Locate and identify every blood parasite.
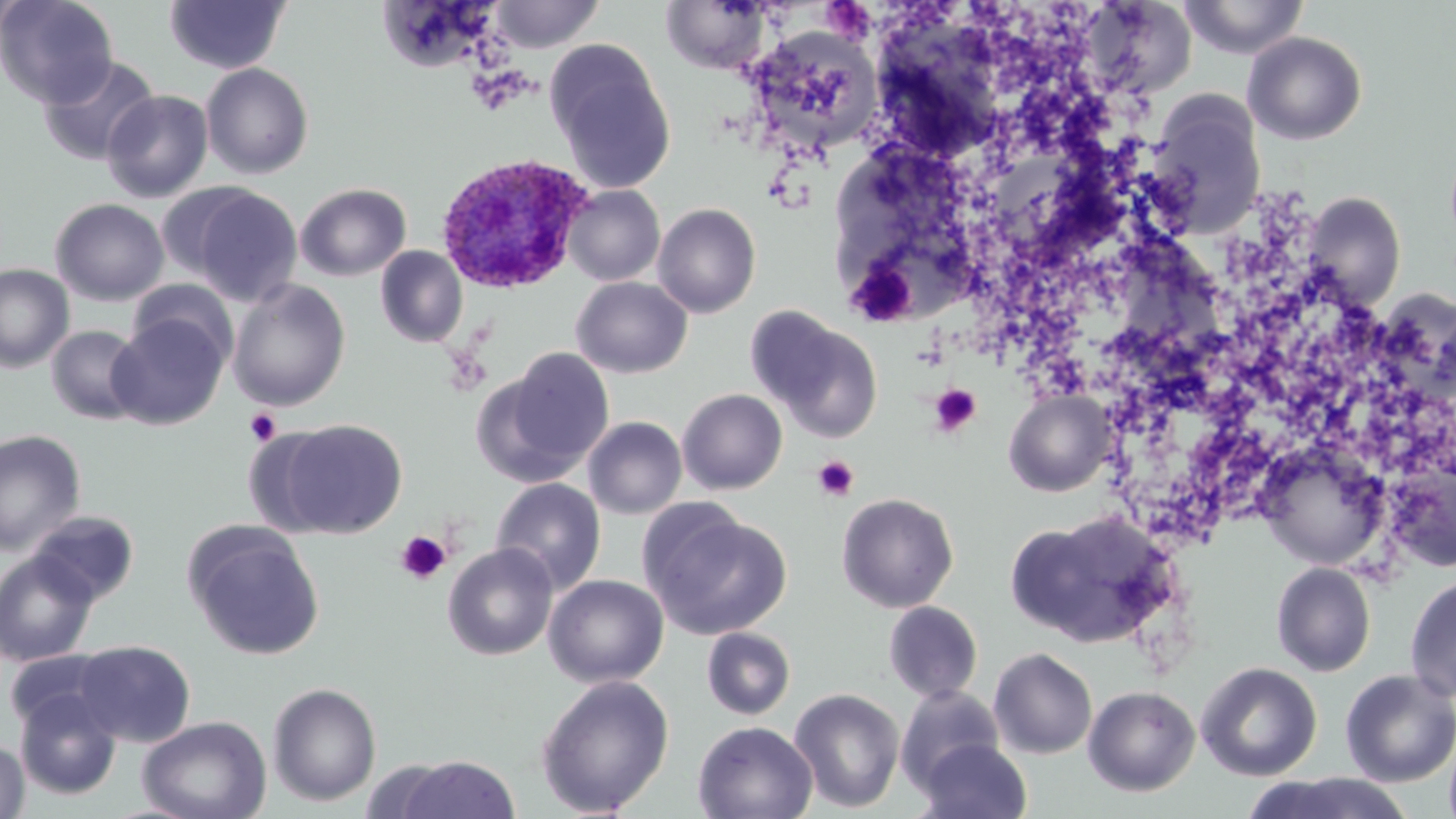
Approximate bounding boxes as (x1, y1, x2, y2) in pixels.
Plasmodium ovale-infected red blood cells: (434, 152, 593, 295).
No Plasmodium falciparum, Plasmodium malariae, Plasmodium vivax, Babesia divergens, or Trypanosoma brucei observed.

slide-level diagnosis = Plasmodium ovale
uninfected red blood cell locations = approximate bounding boxes as (x1, y1, x2, y2) in pixels: (1, 0, 117, 107), (163, 0, 290, 75), (1178, 0, 1310, 60), (489, 1, 604, 52), (660, 1, 769, 74), (744, 25, 883, 154), (1242, 31, 1368, 145), (546, 42, 677, 195), (37, 55, 160, 166), (201, 63, 314, 179), (101, 89, 213, 202), (1148, 98, 1265, 234), (296, 183, 411, 281), (181, 184, 303, 307), (562, 185, 664, 286), (1301, 191, 1406, 311), (50, 198, 169, 306), (653, 203, 761, 318), (375, 245, 468, 347), (0, 263, 74, 373), (571, 277, 692, 378), (128, 280, 239, 371), (227, 280, 351, 411), (751, 309, 884, 441), (107, 312, 229, 430), (45, 324, 146, 425), (489, 348, 615, 481), (678, 389, 787, 494), (583, 417, 687, 519), (272, 418, 408, 538), (0, 429, 86, 555), (1257, 442, 1389, 570), (1384, 455, 1456, 573), (490, 478, 607, 595), (836, 492, 959, 613), (641, 505, 793, 640), (28, 510, 139, 605), (1007, 512, 1171, 647), (185, 523, 325, 661), (443, 543, 558, 661), (1, 549, 100, 667), (1271, 562, 1375, 676), (1404, 573, 1456, 704), (543, 575, 669, 689), (883, 601, 983, 702), (701, 627, 795, 720), (74, 640, 195, 746), (4, 648, 120, 736), (988, 648, 1098, 759), (1196, 662, 1322, 781), (1339, 668, 1456, 786), (536, 675, 674, 817), (267, 682, 381, 807), (894, 685, 1005, 795), (1083, 685, 1200, 797), (14, 688, 122, 800), (789, 688, 905, 814), (137, 714, 272, 819), (692, 721, 817, 819), (0, 737, 30, 819), (915, 738, 1033, 819), (387, 755, 522, 818), (1241, 771, 1416, 819)
magnification = 1000x
preparation = thin blood smear
image size = 1456×819 pixels
platelet locations = approximate bounding boxes as (x1, y1, x2, y2) in pixels: (929, 384, 981, 437), (245, 408, 281, 445), (812, 456, 860, 502), (395, 531, 452, 585)
field of view = one of a larger specimen
stain = May-Grünwald-Giemsa
modality = light microscopy